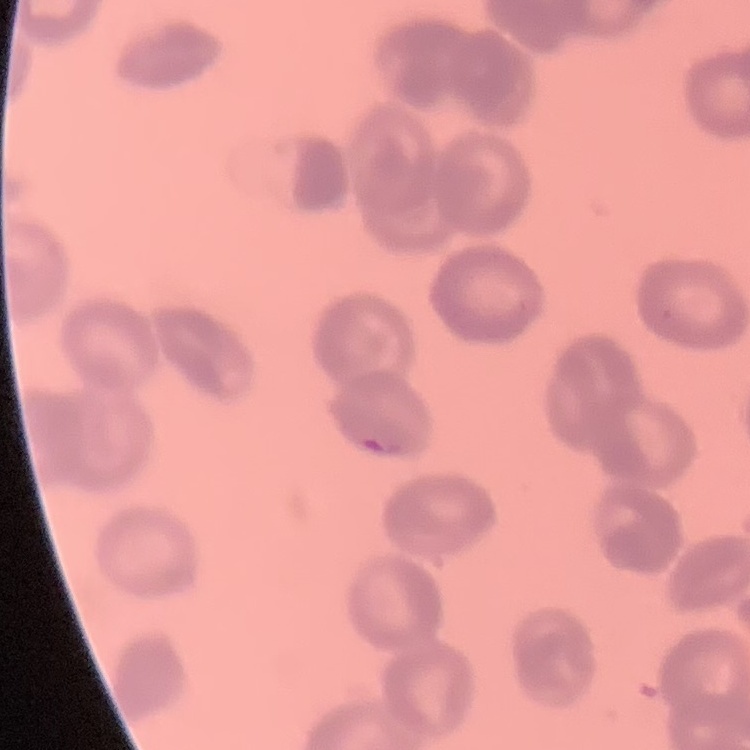
The red blood cells show rouleaux formation. Stained with either Field's or Giemsa. Thin blood film. One tile cut from a larger photomicrograph.